Classify this cell by malaria status.
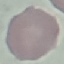

Uninfected.

Automatically extracted cell patch, resized to 64 × 64 pixels. Thin smear of blood. Giemsa stain. Acquired by smartphone through the microscope eyepiece.